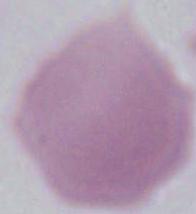

{
  "identification": "red blood cell",
  "magnification": "1000x",
  "modality": "photomicrograph"
}